Identify the parasite.
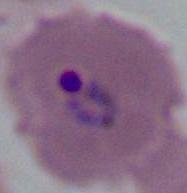

This is Plasmodium.

Summary:
  - Magnification: 400x or 1000x
  - Modality: micrograph